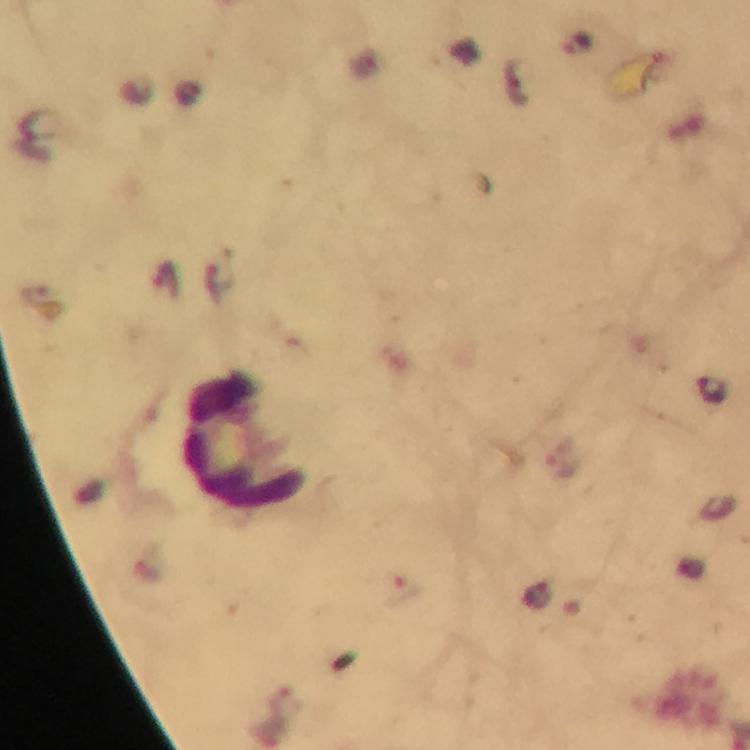
{
  "cropped_from": "a single field of view",
  "stain": "Giemsa",
  "preparation": "thick blood smear",
  "malaria_parasite_locations": "approximate centers as (x, y) in pixels: (576, 43), (712, 389)",
  "image_size": "750×750 pixels",
  "immersion_oil": "applied",
  "magnification": "100x",
  "leukocyte_locations": "approximate centers as (x, y) in pixels: (246, 442)",
  "context": "from a diagnostic examination for malaria",
  "capture": "smartphone photograph through a microscope"
}